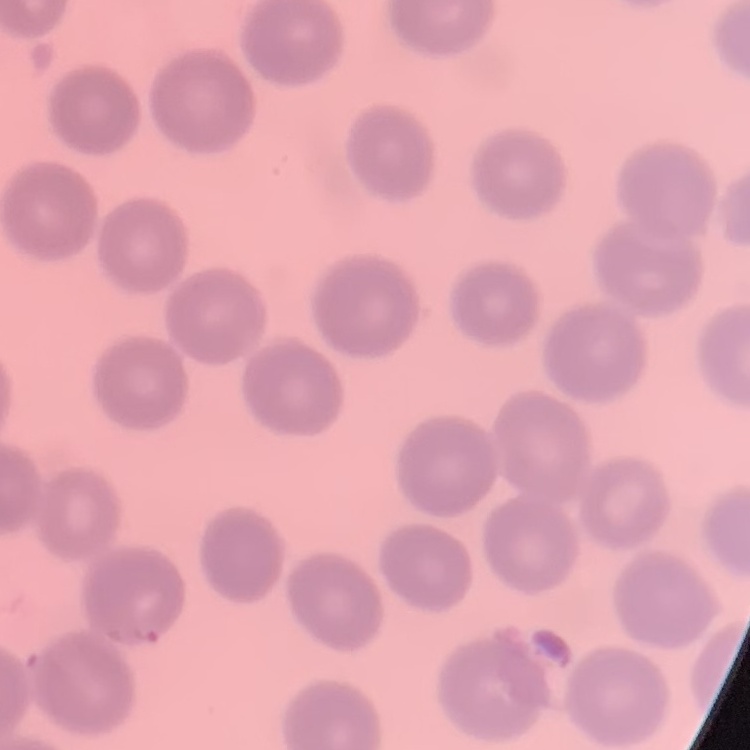
Summary:
  - Erythrocyte morphology: no rouleaux formation
  - Stain: Field's or Giemsa
  - Image type: square crop of a larger photomicrograph
  - Preparation: thin peripheral smear